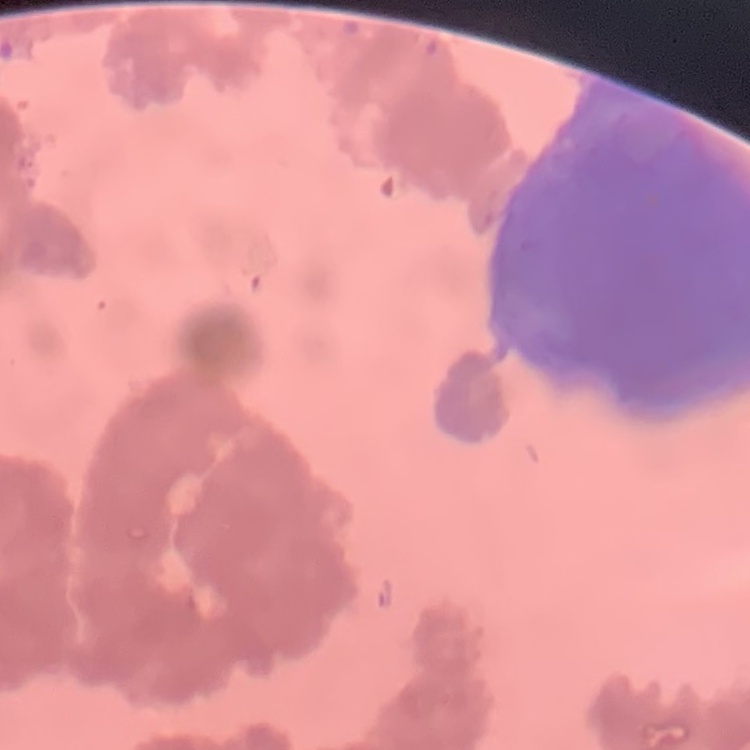
The red blood cells exhibit rouleaux formation. Field's or Giemsa stain. Square crop of a larger photomicrograph. Thin peripheral smear.